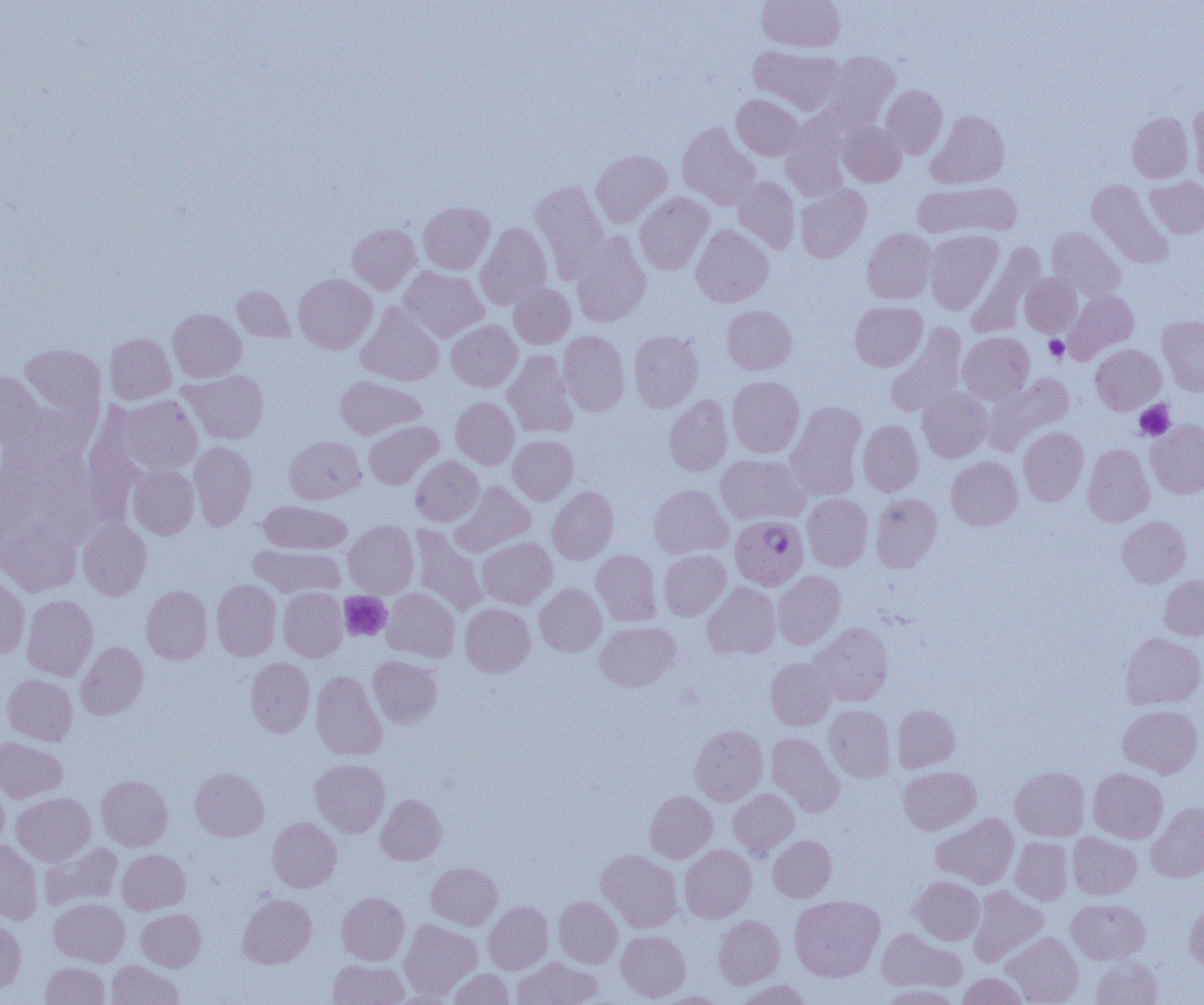

{
  "slide_level_diagnosis": "Plasmodium falciparum",
  "platelet_locations": "approximate bounding boxes as [x1, y1, x2, y2] in pixels: [1044, 335, 1069, 362], [1134, 400, 1175, 440], [339, 591, 392, 641]",
  "uninfected_red_blood_cell_locations": "approximate bounding boxes as [x1, y1, x2, y2] in pixels: [758, 0, 845, 52], [749, 45, 842, 114], [820, 52, 899, 131], [880, 85, 947, 158], [732, 94, 804, 160], [1188, 102, 1204, 184], [926, 110, 1009, 189], [1127, 112, 1193, 182], [781, 116, 850, 202], [837, 121, 906, 187], [678, 122, 760, 210], [591, 150, 672, 227], [734, 176, 800, 254], [1145, 177, 1204, 238], [531, 180, 609, 281], [1087, 180, 1174, 269], [913, 182, 1021, 239], [795, 185, 870, 263], [634, 192, 713, 274], [418, 201, 495, 274], [476, 222, 552, 309], [347, 223, 420, 294], [691, 225, 773, 307], [1046, 228, 1125, 301], [863, 229, 936, 303], [924, 230, 1003, 314], [572, 232, 650, 327], [968, 241, 1045, 336], [399, 265, 489, 342], [294, 273, 377, 353], [1020, 273, 1081, 337], [509, 284, 575, 348], [232, 286, 296, 342], [1065, 290, 1139, 362], [850, 301, 927, 371], [357, 303, 444, 385], [722, 305, 796, 373], [168, 309, 246, 382], [1158, 316, 1204, 395], [446, 320, 522, 391], [886, 324, 967, 418], [628, 330, 703, 412], [558, 331, 629, 416], [958, 332, 1034, 404], [105, 333, 176, 404], [20, 344, 105, 414], [1091, 344, 1166, 414], [502, 350, 578, 438], [180, 370, 269, 444], [0, 371, 45, 448], [985, 373, 1074, 452], [336, 376, 425, 439], [727, 376, 804, 458], [917, 388, 991, 462], [664, 394, 733, 476], [117, 395, 202, 475], [451, 397, 519, 469], [786, 402, 867, 500], [2, 403, 92, 479], [82, 411, 145, 528], [364, 420, 443, 489], [858, 420, 923, 496], [1146, 420, 1204, 498], [1018, 426, 1088, 505], [284, 435, 365, 503], [508, 435, 578, 504], [189, 441, 256, 530], [1083, 444, 1154, 526], [715, 454, 810, 524], [411, 456, 484, 525], [946, 456, 1023, 530], [129, 466, 199, 539], [451, 481, 535, 556], [649, 485, 732, 558], [548, 486, 618, 564], [802, 493, 873, 571], [871, 493, 942, 572], [258, 500, 352, 553], [1117, 515, 1191, 587], [0, 520, 81, 596], [78, 520, 151, 599], [344, 520, 418, 598], [410, 525, 488, 617], [477, 537, 556, 608], [249, 545, 344, 597], [592, 550, 661, 626], [658, 550, 731, 620], [772, 570, 845, 649], [0, 573, 30, 657], [1159, 574, 1204, 640], [212, 579, 281, 660], [703, 582, 780, 659], [535, 584, 606, 655], [141, 585, 212, 664], [279, 587, 347, 661], [382, 588, 460, 662], [22, 595, 98, 680], [460, 603, 535, 677], [596, 622, 679, 691], [809, 622, 893, 706], [1121, 633, 1204, 709], [76, 642, 148, 720], [368, 656, 441, 727], [245, 657, 314, 737], [765, 657, 836, 730], [311, 671, 387, 760], [2, 674, 77, 745], [892, 704, 960, 772], [1118, 704, 1203, 778], [824, 705, 895, 782], [690, 725, 768, 805], [766, 732, 844, 816], [0, 736, 67, 802], [311, 758, 389, 836], [899, 766, 981, 834], [190, 767, 268, 841], [1010, 767, 1089, 840], [1088, 768, 1168, 842], [96, 774, 172, 850], [0, 779, 8, 852], [729, 788, 800, 858], [645, 790, 717, 862], [12, 792, 95, 865], [376, 794, 446, 864], [1146, 802, 1204, 882], [932, 813, 1019, 889], [267, 817, 341, 892], [1068, 832, 1141, 899], [768, 836, 836, 901], [1010, 837, 1073, 905], [0, 840, 42, 924], [40, 842, 123, 910], [680, 844, 756, 923], [117, 849, 190, 915], [597, 849, 683, 932], [426, 862, 502, 929], [911, 876, 984, 944], [968, 885, 1047, 966], [337, 892, 409, 965], [238, 894, 316, 968], [790, 895, 884, 981], [554, 896, 622, 967], [49, 898, 129, 966], [1067, 898, 1150, 964], [1185, 899, 1204, 970], [483, 901, 553, 974], [137, 909, 206, 970], [714, 915, 784, 988], [0, 919, 25, 995], [399, 920, 481, 1000], [877, 928, 966, 992], [616, 930, 690, 1001], [1001, 932, 1083, 1005], [512, 956, 602, 1005], [1091, 956, 1162, 1005], [328, 959, 408, 1005], [107, 960, 184, 1005], [41, 962, 109, 1004], [448, 969, 514, 1005], [957, 973, 1029, 1005], [737, 979, 811, 1005], [878, 985, 963, 1004], [388, 990, 458, 1004], [657, 991, 728, 1004]",
  "field_of_view": "one of a larger specimen",
  "plasmodium_falciparum_infected_red_blood_cell_locations": "approximate bounding boxes as [x1, y1, x2, y2] in pixels: [730, 515, 808, 590]",
  "modality": "optical microscopy",
  "image_size": "1204×1005 pixels",
  "magnification": "1000x",
  "preparation": "thin blood film"
}